State which parasite is depicted.
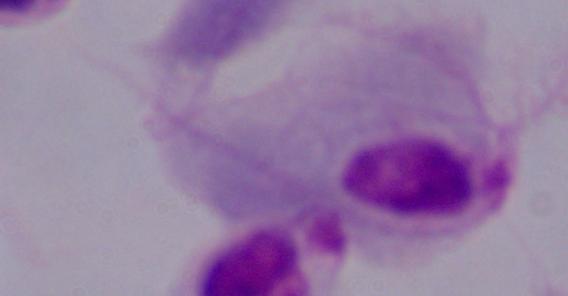

This is a trichomonad.

modality: micrograph
magnification: 1000x